Locate every Plasmodium parasite and identify its life-cycle stage.
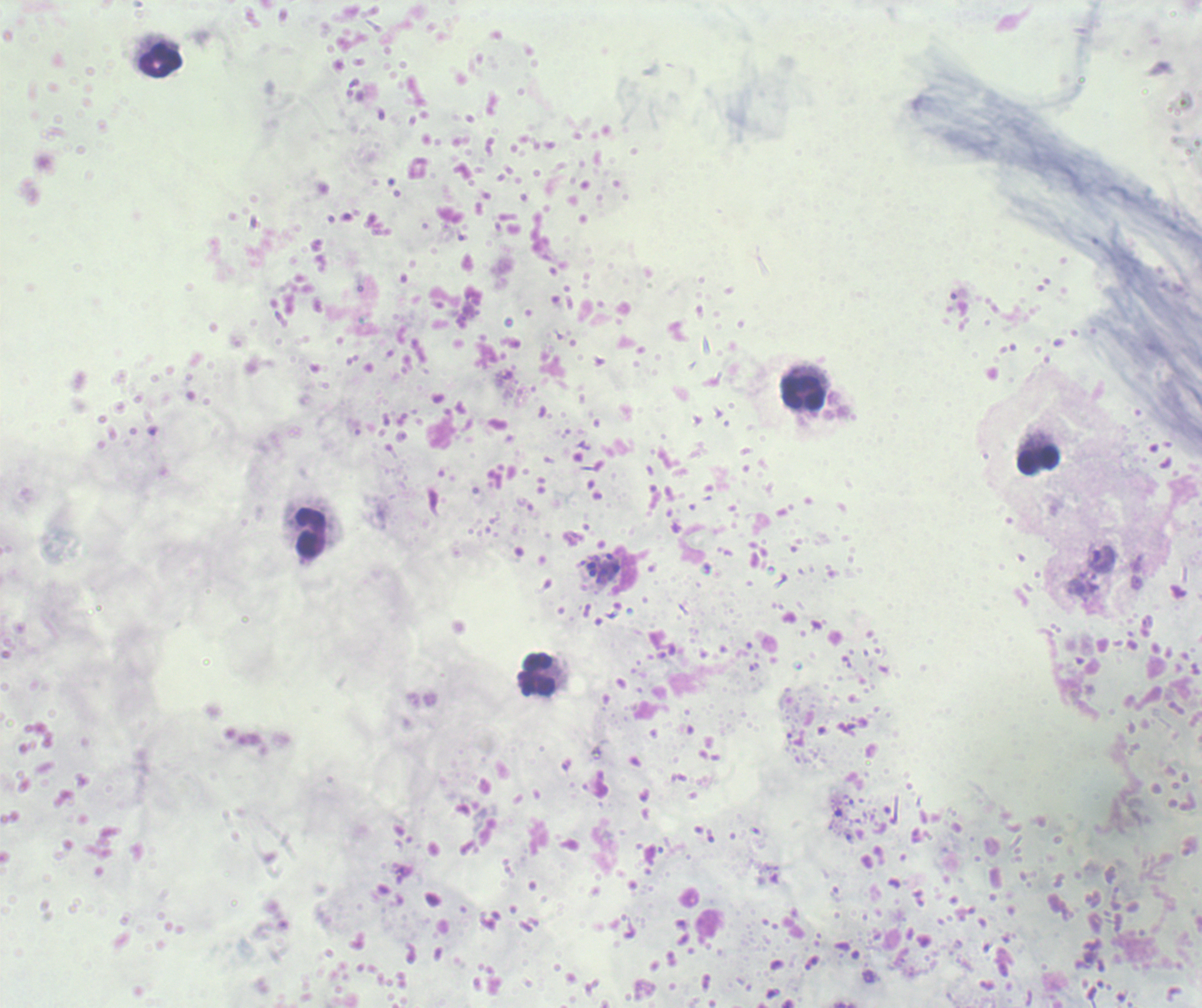
Approximate object centers, in pixels from the top-left corner.
Trophozoites: (x=1103, y=559).
Schizonts: (x=603, y=565).
No gametocyte forms observed.

Approximate object centers, in pixels from the top-left corner.
Summary:
  - Leukocyte locations: (x=161, y=61), (x=802, y=394), (x=1039, y=461), (x=311, y=534), (x=538, y=675)
  - Magnification: 100x
  - Field of view: one from this slide
  - Preparation: thick blood film
  - Background quality: poor
  - Stain: Romanowsky
  - Context: previously used in an actual diagnosis
  - Image size: 1202×1008 pixels